Locate platelets.
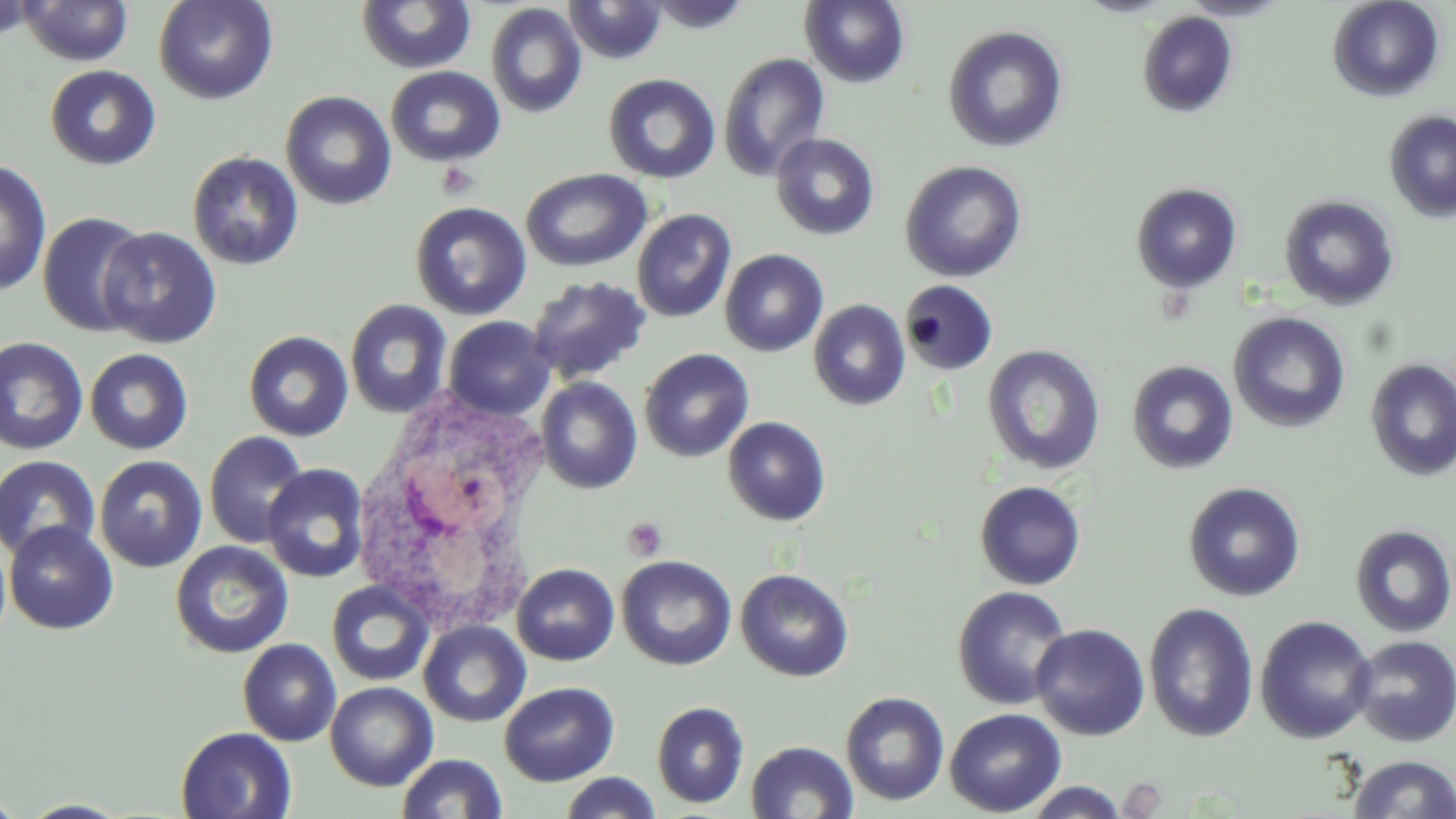
Approximate bounding boxes as named x1/y1/x2/y2 corners in pixels.
Platelets: (x1=436, y1=161, x2=479, y2=200), (x1=623, y1=517, x2=668, y2=560).

White blood cell locations: (x1=347, y1=388, x2=563, y2=633). Uninfected red blood cell locations: (x1=0, y1=0, x2=41, y2=43), (x1=153, y1=0, x2=278, y2=105), (x1=564, y1=0, x2=668, y2=65), (x1=644, y1=0, x2=754, y2=33), (x1=800, y1=0, x2=910, y2=88), (x1=1076, y1=0, x2=1175, y2=17), (x1=1179, y1=0, x2=1293, y2=21), (x1=1328, y1=0, x2=1445, y2=102), (x1=17, y1=1, x2=134, y2=66), (x1=356, y1=1, x2=477, y2=74), (x1=486, y1=3, x2=587, y2=119), (x1=1137, y1=11, x2=1239, y2=118), (x1=942, y1=25, x2=1069, y2=153), (x1=718, y1=52, x2=831, y2=181), (x1=46, y1=64, x2=161, y2=169), (x1=385, y1=66, x2=506, y2=166), (x1=602, y1=73, x2=721, y2=184), (x1=280, y1=91, x2=397, y2=210), (x1=1385, y1=110, x2=1456, y2=222), (x1=770, y1=132, x2=880, y2=240), (x1=187, y1=151, x2=304, y2=270), (x1=0, y1=158, x2=52, y2=297), (x1=900, y1=160, x2=1027, y2=282), (x1=521, y1=167, x2=652, y2=272), (x1=1131, y1=182, x2=1243, y2=293), (x1=1279, y1=195, x2=1400, y2=311), (x1=410, y1=201, x2=532, y2=320), (x1=631, y1=208, x2=737, y2=323), (x1=37, y1=211, x2=152, y2=337), (x1=98, y1=226, x2=222, y2=349), (x1=720, y1=249, x2=829, y2=357), (x1=526, y1=274, x2=652, y2=385), (x1=900, y1=280, x2=998, y2=375), (x1=345, y1=298, x2=453, y2=418), (x1=808, y1=299, x2=910, y2=411), (x1=1228, y1=312, x2=1350, y2=433), (x1=443, y1=316, x2=555, y2=420), (x1=243, y1=330, x2=353, y2=441), (x1=0, y1=336, x2=88, y2=455), (x1=982, y1=344, x2=1106, y2=475), (x1=85, y1=348, x2=194, y2=454), (x1=639, y1=348, x2=755, y2=462), (x1=1365, y1=358, x2=1456, y2=481), (x1=1126, y1=360, x2=1239, y2=474), (x1=535, y1=377, x2=643, y2=494), (x1=722, y1=416, x2=831, y2=526), (x1=203, y1=430, x2=311, y2=548), (x1=0, y1=455, x2=101, y2=561), (x1=94, y1=455, x2=207, y2=572), (x1=262, y1=464, x2=370, y2=583), (x1=974, y1=480, x2=1086, y2=590), (x1=1183, y1=482, x2=1306, y2=602), (x1=3, y1=521, x2=119, y2=635), (x1=1350, y1=524, x2=1456, y2=638), (x1=170, y1=540, x2=294, y2=659), (x1=616, y1=555, x2=737, y2=670), (x1=511, y1=563, x2=619, y2=666), (x1=735, y1=568, x2=855, y2=682), (x1=326, y1=580, x2=434, y2=686), (x1=952, y1=586, x2=1073, y2=710), (x1=1143, y1=602, x2=1260, y2=742), (x1=1255, y1=616, x2=1378, y2=744), (x1=418, y1=620, x2=531, y2=727), (x1=1031, y1=623, x2=1151, y2=741), (x1=1351, y1=635, x2=1456, y2=747), (x1=238, y1=638, x2=342, y2=746), (x1=324, y1=681, x2=438, y2=790), (x1=499, y1=681, x2=619, y2=786), (x1=840, y1=691, x2=950, y2=806), (x1=651, y1=701, x2=750, y2=809), (x1=944, y1=708, x2=1067, y2=817), (x1=175, y1=726, x2=297, y2=819), (x1=745, y1=741, x2=859, y2=819), (x1=397, y1=753, x2=508, y2=818), (x1=1349, y1=755, x2=1455, y2=819), (x1=558, y1=772, x2=661, y2=818), (x1=1022, y1=781, x2=1130, y2=818), (x1=0, y1=792, x2=26, y2=818), (x1=19, y1=800, x2=134, y2=818). Slide-level diagnosis: no evidence of blood parasites. Optical microscopy. Captured at 1000x magnification. May-Grünwald-Giemsa stain. Image is 1456×819 pixels. Single field of view. Thin blood film.